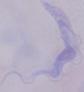

modality = photomicrograph
identification = trypanosome
magnification = 1000x